State the preparation type.
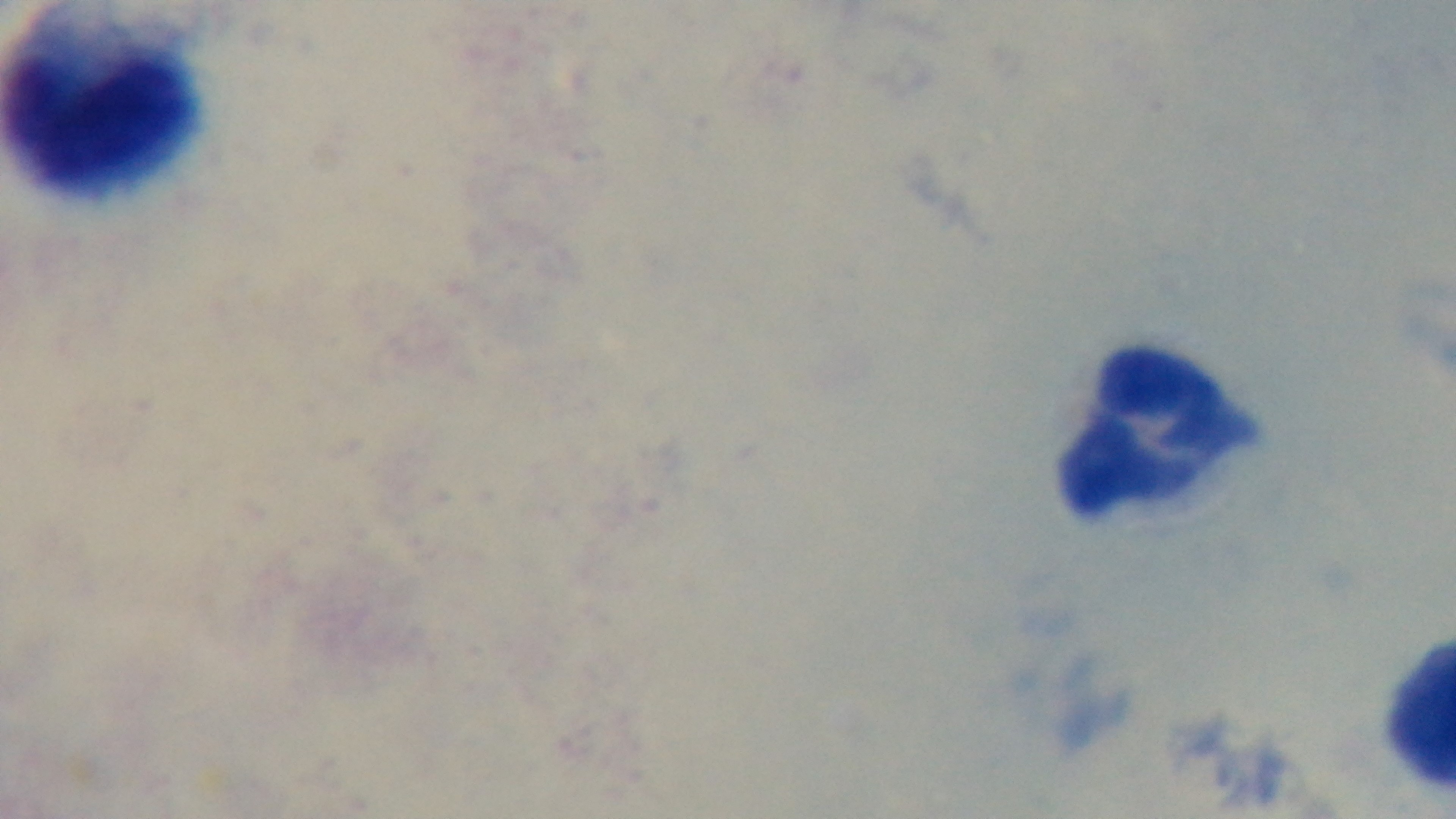
A thick smear.

Giemsa-stained. Oil-immersion objective, 100x. Malaria status: uninfected. Light microscopy. One field from the slide. Captured with a mounted 4K digital camera.